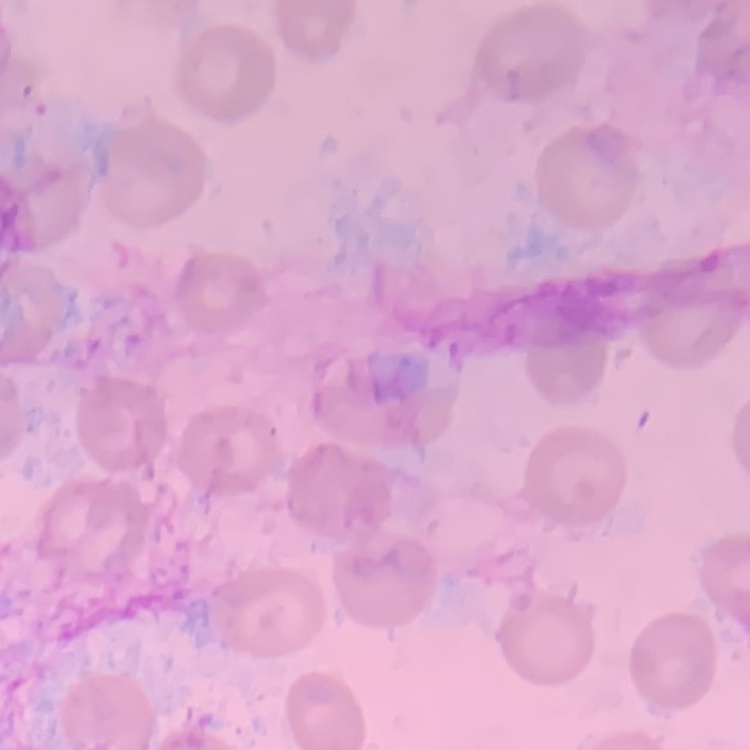
red_blood_cell_morphology: no rouleaux formation
preparation: thin blood smear
stain: Field's or Giemsa
image_type: square crop of a larger photomicrograph